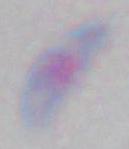

magnification = 1000x
modality = photomicrograph
identification = Toxoplasma gondii